Classify this cell by malaria status.
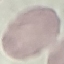
It is uninfected.

Summary:
  - Capture: smartphone camera at the microscope eyepiece
  - Stain: Giemsa
  - Image type: cell patch, automatically extracted from a larger field of view and resized to 64 × 64 pixels
  - Preparation: thin blood film